State which parasite is depicted.
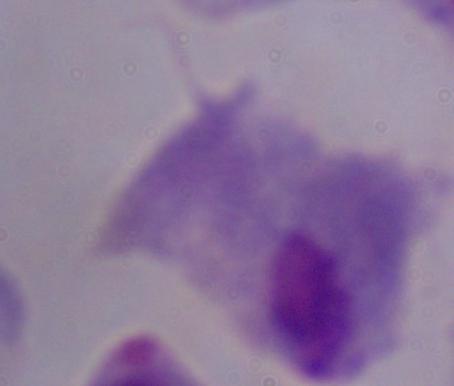
This is a trichomonad.

Captured at 1000x magnification. Micrograph.